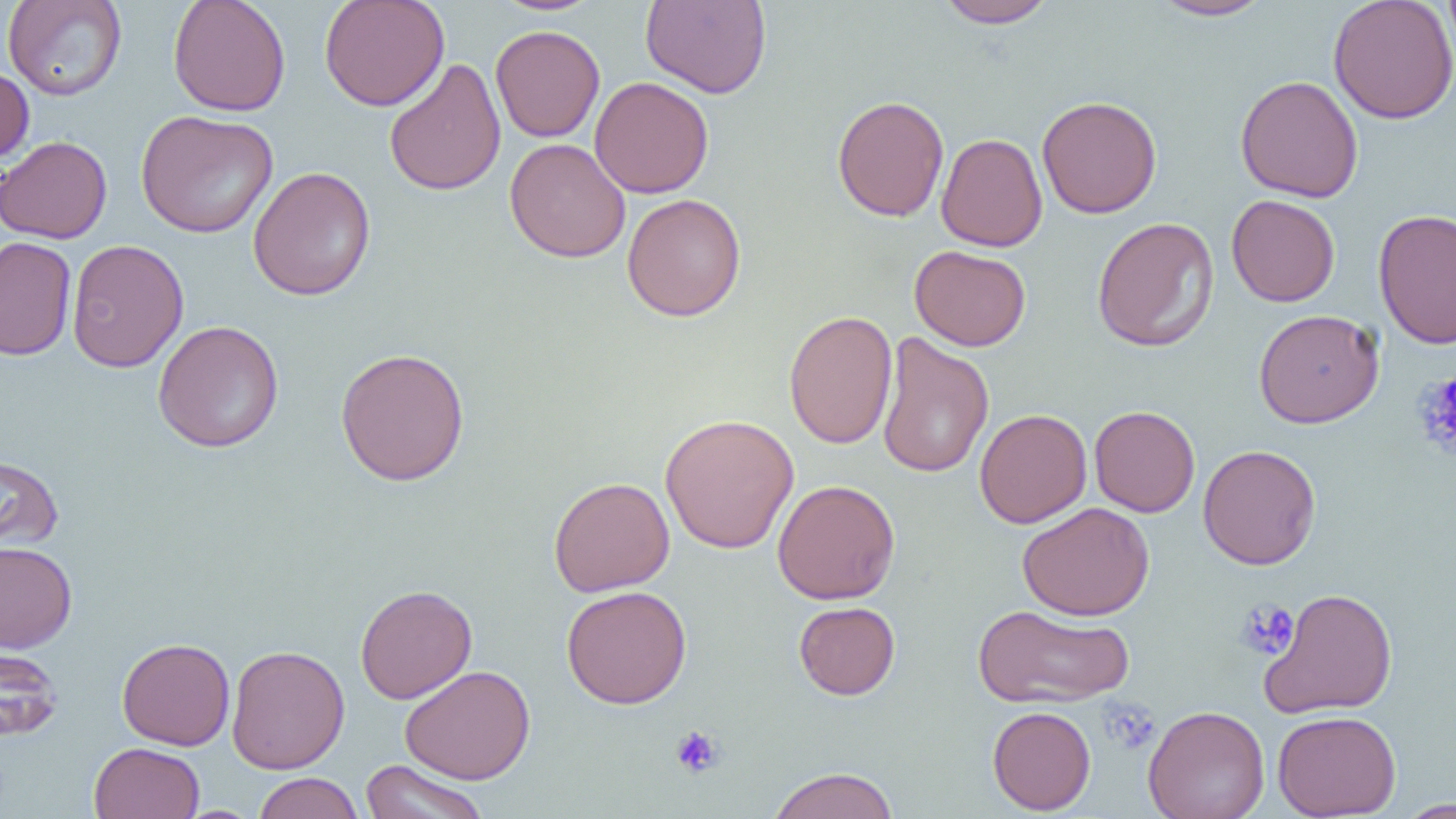
slide_level_diagnosis: no evidence of blood parasites
platelet_locations: 'approximate bounding boxes as [x1, y1, x2, y2] in pixels: [1413, 371, 1456, 460], [1235, 599, 1299, 660], [1101, 700, 1161, 755], [670, 725, 724, 778]'
preparation: thin blood film
magnification: 1000x
field_of_view: one of a larger specimen
image_size: 1456×819 pixels
uninfected_red_blood_cell_locations: 'approximate bounding boxes as [x1, y1, x2, y2] in pixels: [2, 0, 128, 101], [167, 0, 291, 116], [319, 0, 450, 112], [492, 0, 604, 16], [1328, 0, 1456, 124], [1443, 0, 1456, 68], [640, 1, 772, 99], [935, 1, 1059, 29], [1148, 1, 1274, 21], [490, 24, 605, 142], [384, 58, 506, 197], [0, 65, 35, 164], [1235, 74, 1364, 203], [589, 76, 714, 199], [831, 94, 950, 221], [1036, 95, 1163, 218], [136, 109, 278, 238], [936, 133, 1048, 252], [0, 135, 112, 244], [505, 138, 631, 263], [248, 166, 376, 301], [621, 193, 747, 322], [1226, 194, 1340, 307], [1373, 208, 1456, 350], [1091, 216, 1220, 352], [0, 236, 77, 361], [66, 239, 189, 372], [909, 245, 1031, 351], [1253, 308, 1384, 428], [783, 310, 898, 449], [152, 320, 284, 453], [876, 332, 994, 480], [335, 346, 470, 486], [1088, 405, 1200, 517], [974, 408, 1092, 528], [660, 413, 800, 554], [1198, 444, 1321, 570], [0, 454, 64, 554], [548, 476, 675, 597], [772, 479, 900, 604], [1017, 502, 1155, 621], [0, 541, 78, 652], [354, 584, 478, 704], [561, 585, 692, 709], [1258, 587, 1398, 718], [793, 601, 901, 700], [971, 604, 1134, 708], [117, 637, 235, 750], [0, 644, 63, 742], [226, 644, 350, 774], [399, 665, 536, 785], [1143, 705, 1270, 819], [987, 706, 1096, 814], [1271, 709, 1402, 818], [89, 742, 205, 819], [359, 759, 490, 819], [766, 767, 900, 819], [253, 772, 363, 819], [1395, 798, 1456, 818]'
modality: light microscopy